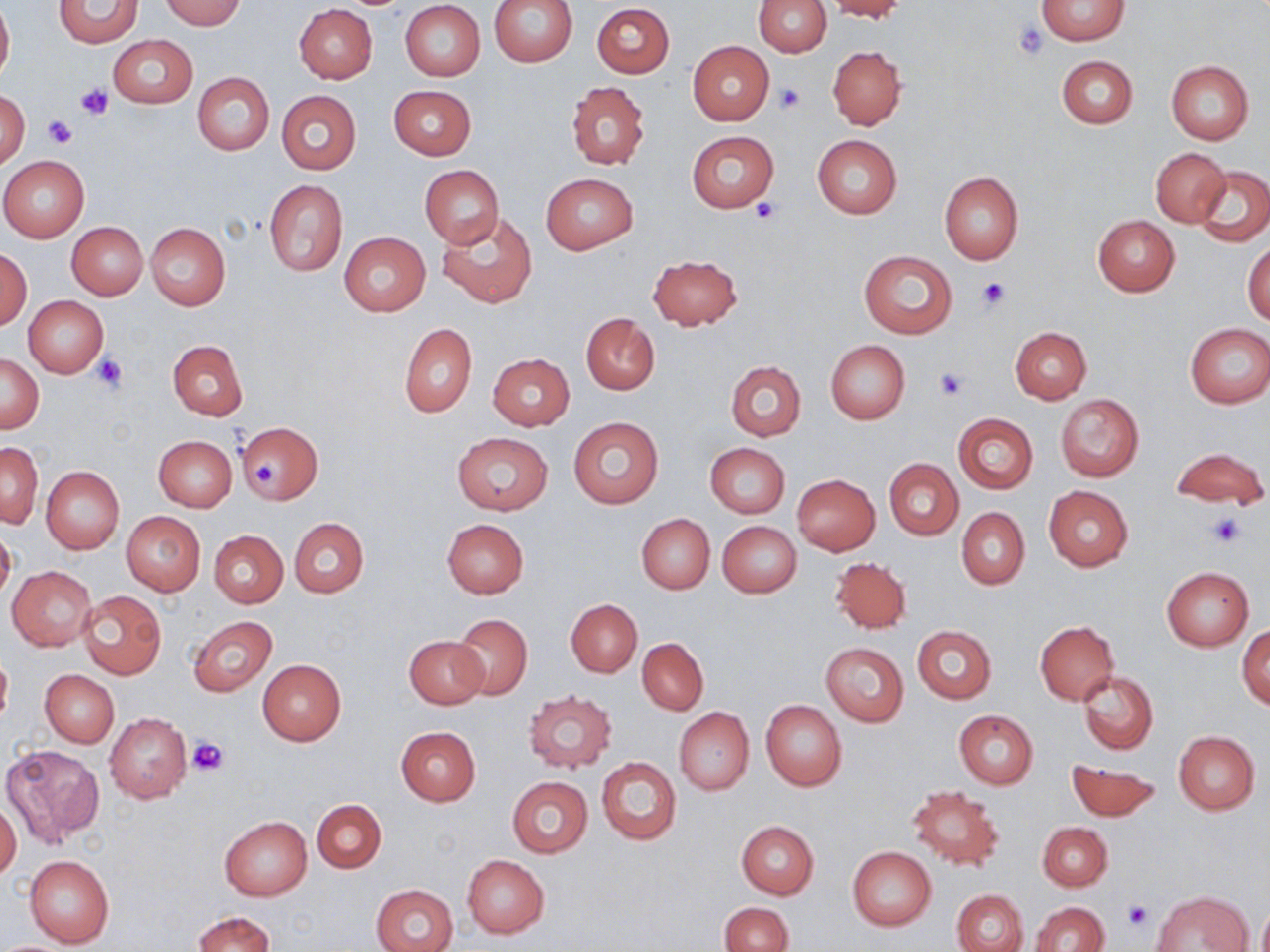

Approximate bounding boxes as (x1,y1)-(x2,y2) corner pairs in pixels. Uninfected red blood cell locations: (160,0)-(245,29), (488,0)-(578,66), (753,0)-(830,56), (824,0)-(907,20), (1036,0)-(1130,45), (0,1)-(13,85), (53,1)-(145,47), (400,2)-(485,81), (591,3)-(674,79), (294,4)-(378,83), (108,35)-(198,108), (687,41)-(775,125), (828,45)-(907,129), (1057,54)-(1138,129), (1167,60)-(1253,145), (194,72)-(274,155), (566,82)-(650,169), (389,85)-(476,159), (276,90)-(361,175), (0,91)-(30,167), (687,131)-(778,213), (812,134)-(901,218), (1151,147)-(1230,226), (1,155)-(89,242), (420,165)-(504,246), (1194,167)-(1270,246), (939,172)-(1023,265), (541,173)-(638,255), (263,178)-(347,276), (437,209)-(537,307), (1092,215)-(1180,297), (66,221)-(148,299), (146,223)-(230,309), (338,232)-(429,316), (1244,242)-(1270,324), (0,249)-(32,329), (859,250)-(958,339), (648,253)-(743,330), (24,295)-(108,377), (580,313)-(660,394), (398,322)-(477,418), (1184,323)-(1269,407), (1010,326)-(1091,404), (168,340)-(248,419), (825,340)-(910,423), (487,353)-(575,431), (0,354)-(44,432), (725,360)-(805,441), (1055,394)-(1144,481), (953,413)-(1037,494), (568,417)-(663,509), (237,420)-(323,504), (453,431)-(553,515), (154,435)-(237,511), (705,442)-(790,517), (1,443)-(43,527), (1167,447)-(1269,509), (884,458)-(963,540), (42,466)-(124,553), (792,473)-(880,554), (1044,485)-(1133,571), (956,507)-(1030,589), (122,511)-(206,596), (637,513)-(715,595), (289,517)-(368,598), (442,518)-(529,598), (718,522)-(801,598), (0,526)-(16,605), (210,530)-(287,607), (831,557)-(912,635), (7,566)-(97,650), (1162,566)-(1253,651), (78,590)-(167,679), (566,599)-(642,677), (451,613)-(532,700), (186,615)-(278,697), (1035,621)-(1118,705), (912,625)-(996,703), (1237,627)-(1270,709), (404,634)-(487,708), (637,638)-(708,715), (820,642)-(909,727), (0,648)-(12,729), (258,659)-(346,745), (40,669)-(119,747), (1079,671)-(1158,755), (524,691)-(617,771), (761,700)-(846,791), (673,708)-(754,795), (954,710)-(1039,789), (105,712)-(192,803), (396,726)-(481,805), (1173,730)-(1261,814), (2,744)-(103,846), (596,756)-(681,845), (1066,761)-(1162,821), (506,776)-(593,858), (907,785)-(1005,871), (312,799)-(386,873), (0,801)-(22,881), (219,816)-(312,900), (736,821)-(819,898), (1037,822)-(1112,890), (848,846)-(936,930), (24,854)-(114,948), (462,855)-(549,938), (371,883)-(457,952), (951,889)-(1026,952), (1151,889)-(1252,952), (1257,900)-(1270,952), (1030,901)-(1110,952), (719,902)-(792,952), (193,911)-(274,952). Platelet locations: (1014,22)-(1049,59), (775,82)-(806,114), (76,84)-(112,120), (41,113)-(78,148), (752,199)-(781,223), (978,278)-(1010,310), (91,352)-(129,394), (934,366)-(970,399), (255,460)-(276,487), (1207,511)-(1245,548), (186,736)-(230,776), (1123,901)-(1153,932). Slide-level diagnosis: no evidence of blood parasites. Captured at 1000x magnification. Image is 1270×952 pixels. One field of a larger specimen. Thin blood film. Optical microscopy. May-Grünwald-Giemsa stain.